Give the extent of all uninfected red blood cells.
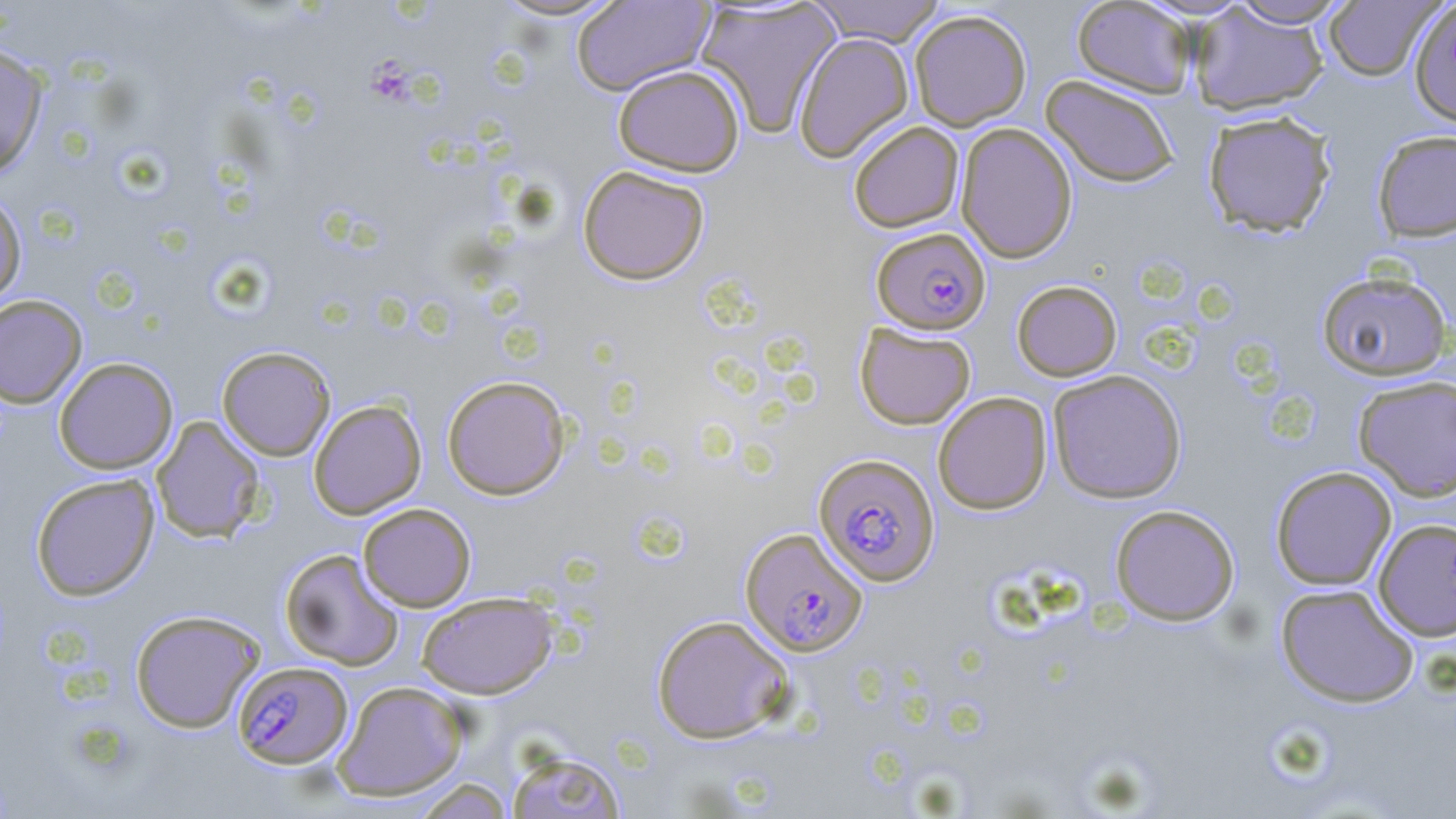

Approximate bounding boxes as (x1,y1)-(x2,y2) corner pairs in pixels.
Uninfected red blood cells: (489,0)-(629,22), (571,0)-(715,95), (807,0)-(948,46), (1071,0)-(1197,98), (1225,0)-(1353,28), (1322,0)-(1442,81), (695,1)-(841,137), (1408,1)-(1456,127), (1188,5)-(1329,116), (909,9)-(1032,131), (793,31)-(914,163), (0,45)-(48,178), (612,64)-(745,177), (1041,75)-(1180,188), (1202,109)-(1337,237), (848,121)-(964,232), (955,122)-(1077,264), (1372,129)-(1456,241), (577,164)-(710,285), (0,189)-(27,306), (1316,270)-(1452,381), (1011,279)-(1122,381), (0,294)-(86,408), (855,323)-(976,429), (216,345)-(336,461), (53,357)-(178,474), (1047,369)-(1187,503), (442,375)-(571,500), (1353,375)-(1456,501), (933,392)-(1052,515), (308,398)-(427,520), (151,416)-(266,544), (1270,466)-(1397,590), (30,473)-(159,601), (357,503)-(476,612), (1110,504)-(1240,626), (1373,517)-(1456,641), (279,548)-(405,670), (1275,583)-(1419,707), (417,591)-(558,699), (129,609)-(265,733), (651,614)-(795,744), (331,680)-(469,801), (505,748)-(627,819), (411,778)-(514,818).

Summary:
  - Plasmodium falciparum-infected red blood cell locations: (872,228)-(990,334), (814,453)-(939,586), (740,527)-(867,657), (233,661)-(352,769)
  - Platelet locations: (371,63)-(418,107)
  - Slide-level diagnosis: Plasmodium falciparum
  - Field of view: one of a larger specimen
  - Magnification: 1000x
  - Stain: May-Grünwald-Giemsa
  - Modality: optical microscopy
  - Image size: 1456×819 pixels
  - Preparation: thin blood smear